Classify this cell by malaria status.
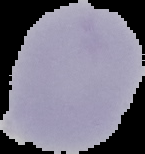
Uninfected.

From a thin blood film. Segmented cell region on a black background. Image is 145×154 pixels.